Locate every Plasmodium parasite.
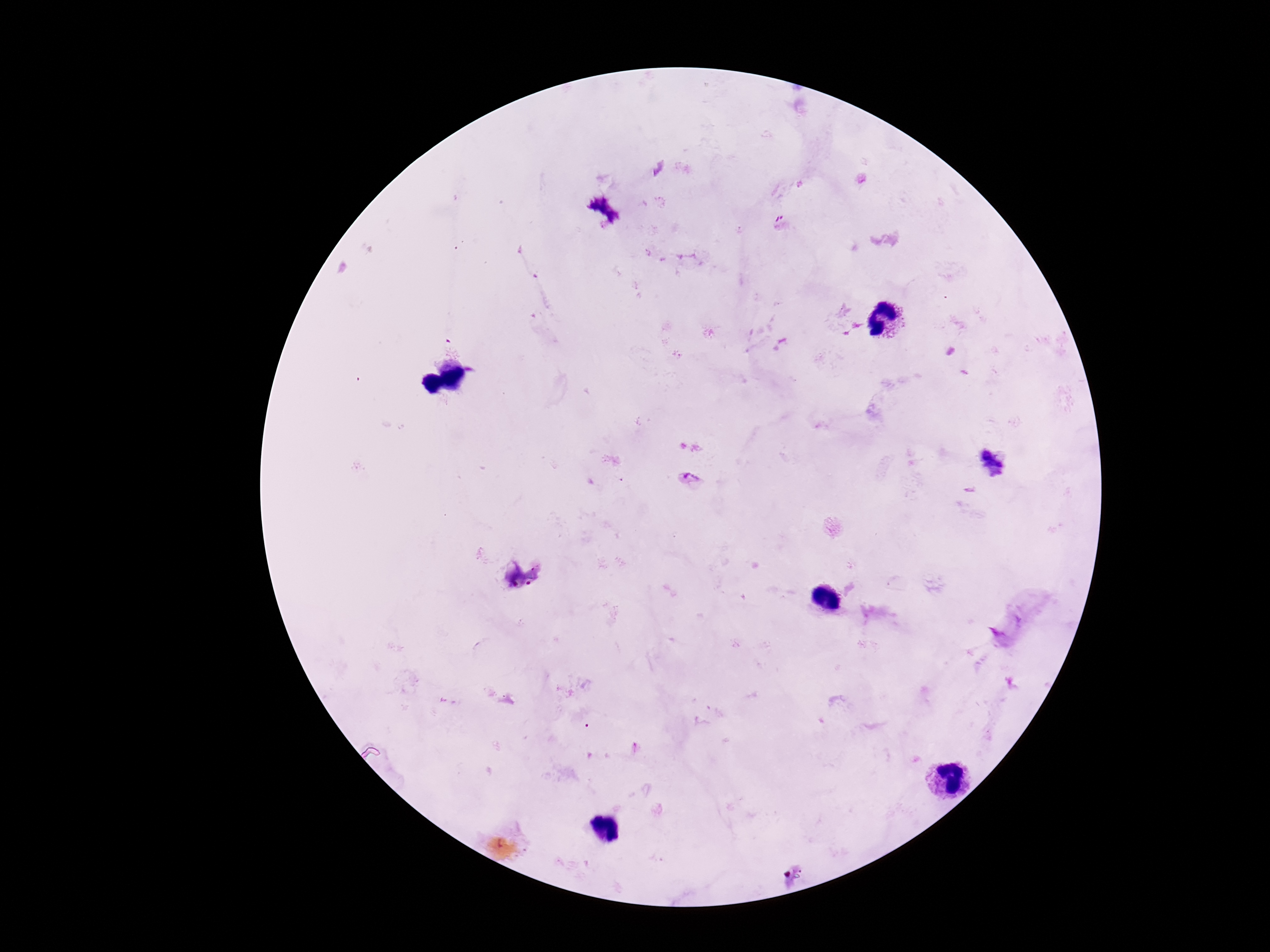

Approximate object centers, in pixels from the top-left corner.
Plasmodium parasites: (x=690, y=479), (x=635, y=749).

Summary:
  - Preparation: thick blood smear
  - Image size: 1270×952 pixels
  - Field of view: single
  - Patient malaria status: positive
  - Stain: Giemsa
  - Magnification: 100x
  - Capture: smartphone camera through the microscope eyepiece